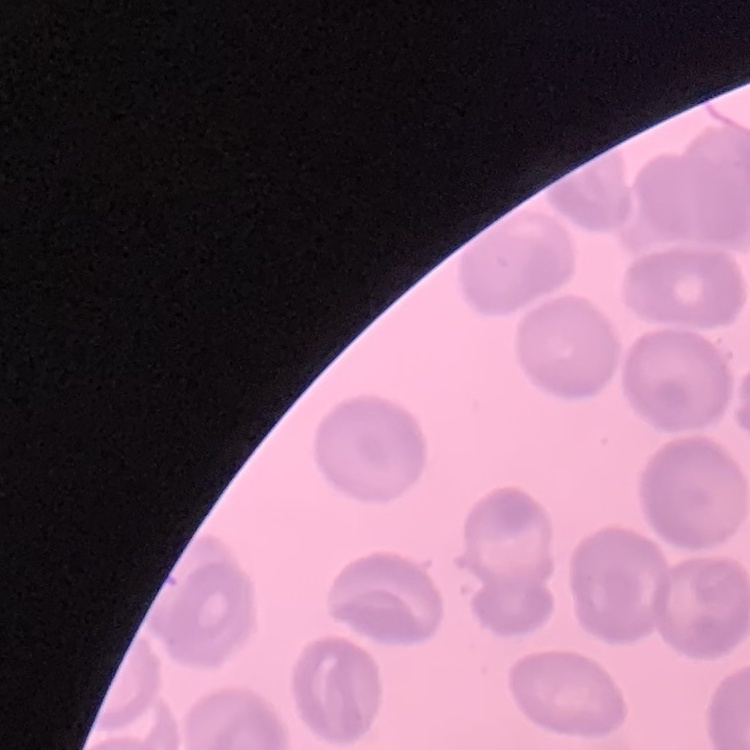 The erythrocytes exhibit no rouleaux formation. Thin peripheral smear. Stained with either Field's or Giemsa. Square crop of a larger photomicrograph.